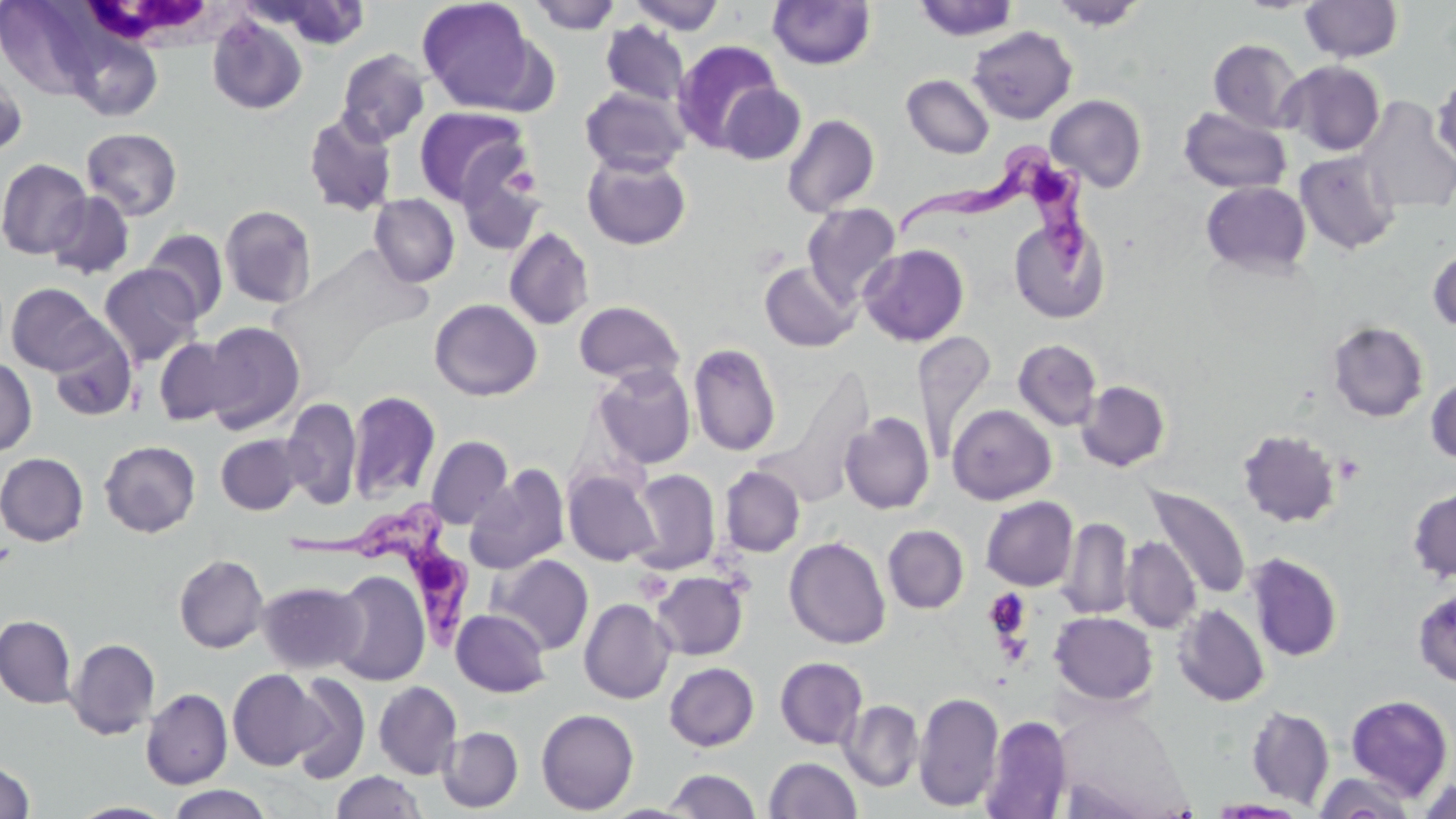

Trypanosoma brucei locations = approximate bounding boxes as (x1,y1)-(x2,y2) corner pairs in pixels: (892,145)-(1097,281), (284,506)-(475,650)
slide-level diagnosis = Trypanosoma brucei
magnification = 1000x
preparation = thin blood smear
image size = 1456×819 pixels
stain = May-Grünwald-Giemsa
modality = light microscopy
uninfected red blood cell locations = approximate bounding boxes as (x1,y1)-(x2,y2) corner pairs in pixels: (416,0)-(540,114), (626,0)-(727,34), (913,0)-(1019,41), (1049,0)-(1149,31), (1300,0)-(1403,63), (265,1)-(371,51), (527,1)-(622,34), (767,1)-(875,69), (207,15)-(308,116), (600,21)-(690,107), (967,25)-(1077,124), (78,39)-(170,125), (1208,39)-(1306,133), (672,40)-(782,152), (336,48)-(430,147), (1281,60)-(1385,157), (0,61)-(27,160), (902,74)-(995,159), (1432,77)-(1456,168), (719,83)-(806,165), (579,85)-(691,177), (1045,94)-(1147,192), (1356,96)-(1456,215), (413,105)-(533,208), (1179,106)-(1292,195), (303,111)-(399,217), (782,114)-(880,217), (82,127)-(183,220), (1295,150)-(1401,256), (582,152)-(692,251), (0,158)-(93,259), (456,161)-(547,257), (1201,181)-(1312,277), (45,190)-(136,279), (369,194)-(459,287), (801,203)-(901,306), (219,205)-(316,308), (1009,216)-(1110,324), (504,227)-(594,330), (143,228)-(229,322), (859,244)-(969,346), (1428,246)-(1456,333), (760,261)-(860,352), (99,264)-(203,366), (6,283)-(110,377), (429,298)-(542,401), (573,300)-(686,385), (201,321)-(306,434), (1327,321)-(1428,422), (48,328)-(138,422), (913,331)-(997,459), (154,336)-(243,426), (1013,339)-(1102,431), (688,343)-(782,456), (0,357)-(37,456), (732,361)-(845,482), (593,364)-(696,470), (771,367)-(874,504), (1425,376)-(1456,465), (1077,380)-(1170,472), (346,390)-(441,504), (282,396)-(362,510), (947,404)-(1056,504), (840,412)-(935,514), (1237,429)-(1342,527), (216,434)-(302,515), (426,435)-(513,530), (99,440)-(200,537), (0,452)-(88,546), (464,464)-(569,575), (720,466)-(805,557), (563,469)-(660,567), (630,469)-(721,574), (1146,484)-(1251,600), (1407,487)-(1456,583), (981,496)-(1078,591), (1059,517)-(1134,619), (883,525)-(969,614), (784,536)-(891,649), (1121,536)-(1201,633), (1246,553)-(1342,661), (174,554)-(269,653), (490,554)-(594,655), (651,570)-(749,660), (330,571)-(430,686), (257,580)-(367,674), (1413,587)-(1456,687), (579,597)-(675,704), (1173,604)-(1269,707), (451,608)-(551,697), (1050,611)-(1158,705), (0,614)-(77,708), (67,638)-(160,739), (774,657)-(867,749), (664,662)-(759,751), (228,669)-(325,770), (287,672)-(371,783), (374,681)-(462,779), (141,688)-(233,788), (914,692)-(1004,812), (1344,694)-(1454,800), (840,699)-(924,791), (1246,705)-(1334,809), (535,707)-(639,814), (981,715)-(1072,818), (438,727)-(523,812), (764,757)-(862,818), (0,760)-(35,818), (665,768)-(761,819), (331,771)-(426,819), (1314,772)-(1417,818), (1419,776)-(1456,819), (165,785)-(274,818), (1205,799)-(1311,817), (68,801)-(176,819)
white blood cell locations = approximate bounding boxes as (x1,y1)-(x2,y2) corner pairs in pixels: (76,1)-(241,51)
platelet locations = approximate bounding boxes as (x1,y1)-(x2,y2) corner pairs in pixels: (505,165)-(542,197), (635,571)-(674,603), (983,589)-(1031,642)
field of view = single